State which cell type is depicted.
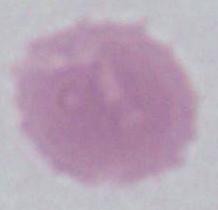
An erythrocyte.

Summary:
  - Magnification: 1000x
  - Modality: micrograph